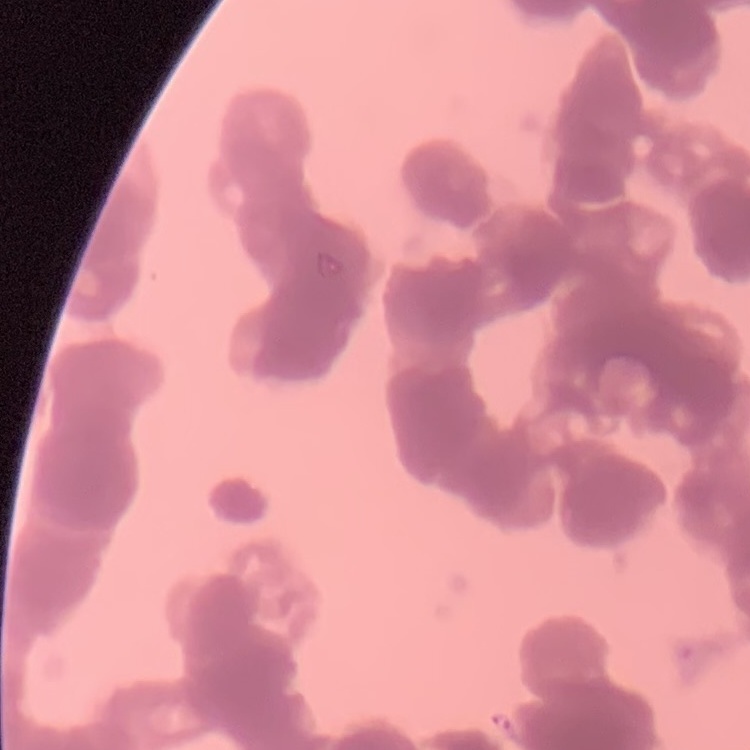

Summary:
  - Erythrocyte morphology: rouleaux formation
  - Preparation: thin peripheral smear
  - Image type: square crop of a larger photomicrograph
  - Stain: Field's or Giemsa